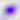
Toxoplasma gondii is shown. 400x magnification. Micrograph.